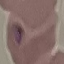
Summary:
  - Result: malaria parasites identified
  - Stain: Giemsa
  - Image type: automatically extracted cell patch, resized to 64 × 64 pixels
  - Capture: smartphone through the microscope eyepiece
  - Preparation: thin blood film